Describe the morphology of the erythrocytes.
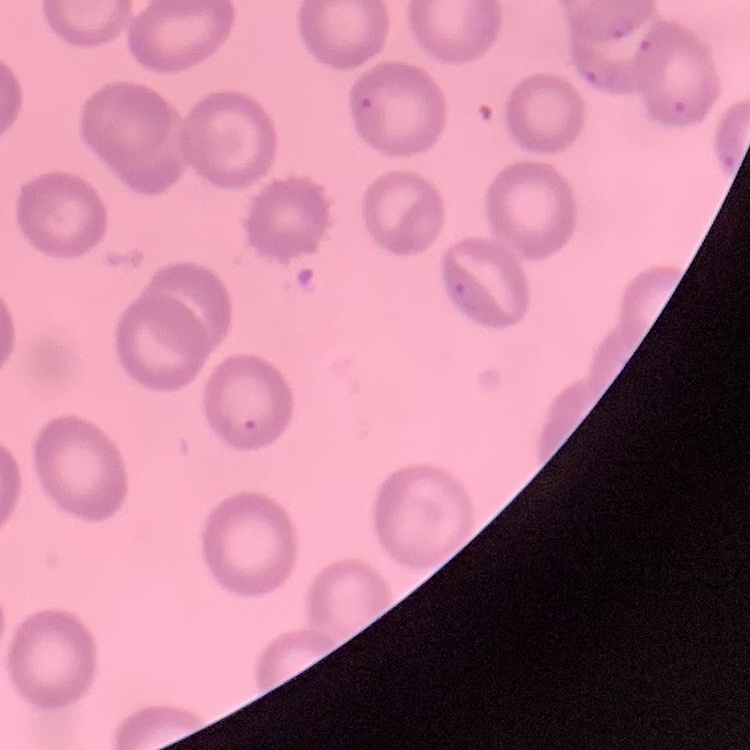

They show no rouleaux formation.

{
  "preparation": "thin blood smear",
  "stain": "Field's or Giemsa",
  "image_type": "square crop of a larger photomicrograph"
}